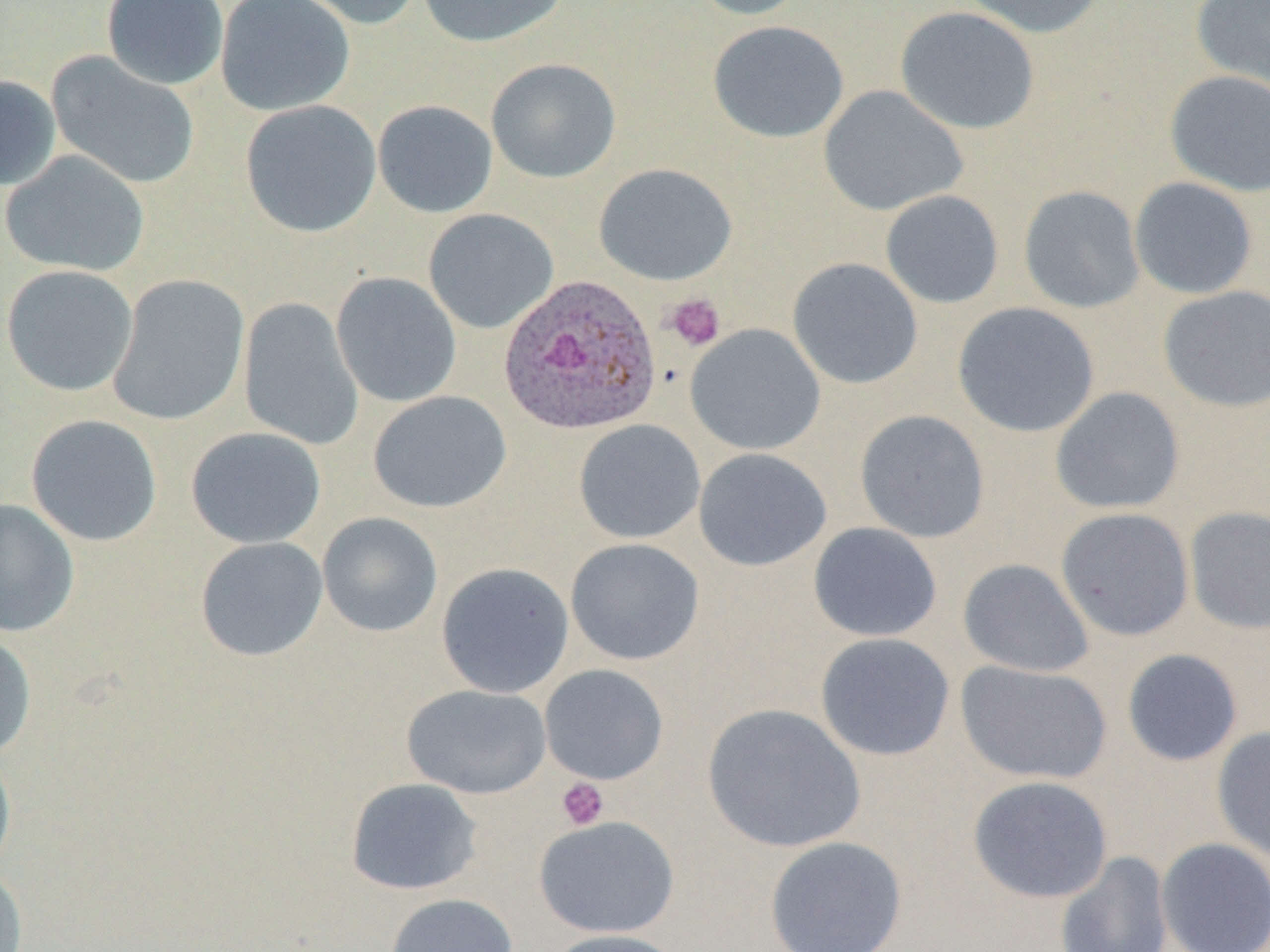
Approximate bounding boxes as named x1/y1/x2/y2 corners in pixels. Platelet locations: (x1=664, y1=293, x2=725, y2=351), (x1=556, y1=777, x2=609, y2=831). Plasmodium ovale-infected red blood cell locations: (x1=498, y1=273, x2=662, y2=436). Uninfected red blood cell locations: (x1=100, y1=0, x2=229, y2=90), (x1=215, y1=0, x2=355, y2=116), (x1=283, y1=0, x2=423, y2=30), (x1=415, y1=0, x2=571, y2=48), (x1=685, y1=0, x2=812, y2=20), (x1=957, y1=0, x2=1107, y2=39), (x1=1190, y1=0, x2=1270, y2=96), (x1=895, y1=6, x2=1040, y2=135), (x1=707, y1=20, x2=849, y2=143), (x1=46, y1=51, x2=200, y2=190), (x1=486, y1=58, x2=621, y2=183), (x1=1165, y1=70, x2=1270, y2=196), (x1=0, y1=75, x2=62, y2=191), (x1=818, y1=84, x2=969, y2=216), (x1=240, y1=100, x2=382, y2=238), (x1=372, y1=100, x2=498, y2=218), (x1=1, y1=150, x2=149, y2=277), (x1=593, y1=163, x2=737, y2=286), (x1=1129, y1=177, x2=1258, y2=300), (x1=1018, y1=185, x2=1145, y2=313), (x1=880, y1=190, x2=1004, y2=309), (x1=423, y1=208, x2=559, y2=334), (x1=786, y1=257, x2=923, y2=390), (x1=1, y1=265, x2=138, y2=396), (x1=330, y1=272, x2=461, y2=408), (x1=107, y1=273, x2=250, y2=427), (x1=1157, y1=285, x2=1270, y2=412), (x1=239, y1=297, x2=364, y2=450), (x1=952, y1=302, x2=1100, y2=438), (x1=685, y1=323, x2=825, y2=455), (x1=1049, y1=386, x2=1185, y2=515), (x1=367, y1=391, x2=512, y2=513), (x1=854, y1=409, x2=991, y2=543), (x1=26, y1=414, x2=162, y2=547), (x1=573, y1=419, x2=705, y2=544), (x1=186, y1=426, x2=327, y2=549), (x1=693, y1=448, x2=832, y2=571), (x1=0, y1=499, x2=80, y2=638), (x1=1185, y1=506, x2=1270, y2=635), (x1=1055, y1=507, x2=1195, y2=642), (x1=317, y1=512, x2=443, y2=637), (x1=808, y1=522, x2=942, y2=642), (x1=195, y1=536, x2=328, y2=662), (x1=565, y1=538, x2=705, y2=666), (x1=957, y1=558, x2=1094, y2=678), (x1=436, y1=562, x2=574, y2=699), (x1=0, y1=630, x2=37, y2=761), (x1=815, y1=632, x2=955, y2=761), (x1=1121, y1=648, x2=1243, y2=767), (x1=954, y1=660, x2=1113, y2=785), (x1=539, y1=664, x2=669, y2=785), (x1=402, y1=684, x2=552, y2=799), (x1=701, y1=703, x2=866, y2=853), (x1=1211, y1=726, x2=1270, y2=862), (x1=0, y1=746, x2=16, y2=878), (x1=966, y1=775, x2=1113, y2=904), (x1=346, y1=778, x2=483, y2=895), (x1=534, y1=815, x2=681, y2=938), (x1=764, y1=835, x2=908, y2=952), (x1=1155, y1=837, x2=1270, y2=952), (x1=1055, y1=850, x2=1174, y2=952), (x1=0, y1=864, x2=28, y2=952), (x1=384, y1=892, x2=519, y2=952), (x1=543, y1=929, x2=687, y2=952). Slide-level diagnosis: Plasmodium ovale. Thin blood film. One field of a larger specimen. Image is 1270×952 pixels. Captured at 1000x magnification. Light microscopy.